Outline each uninfected red blood cell.
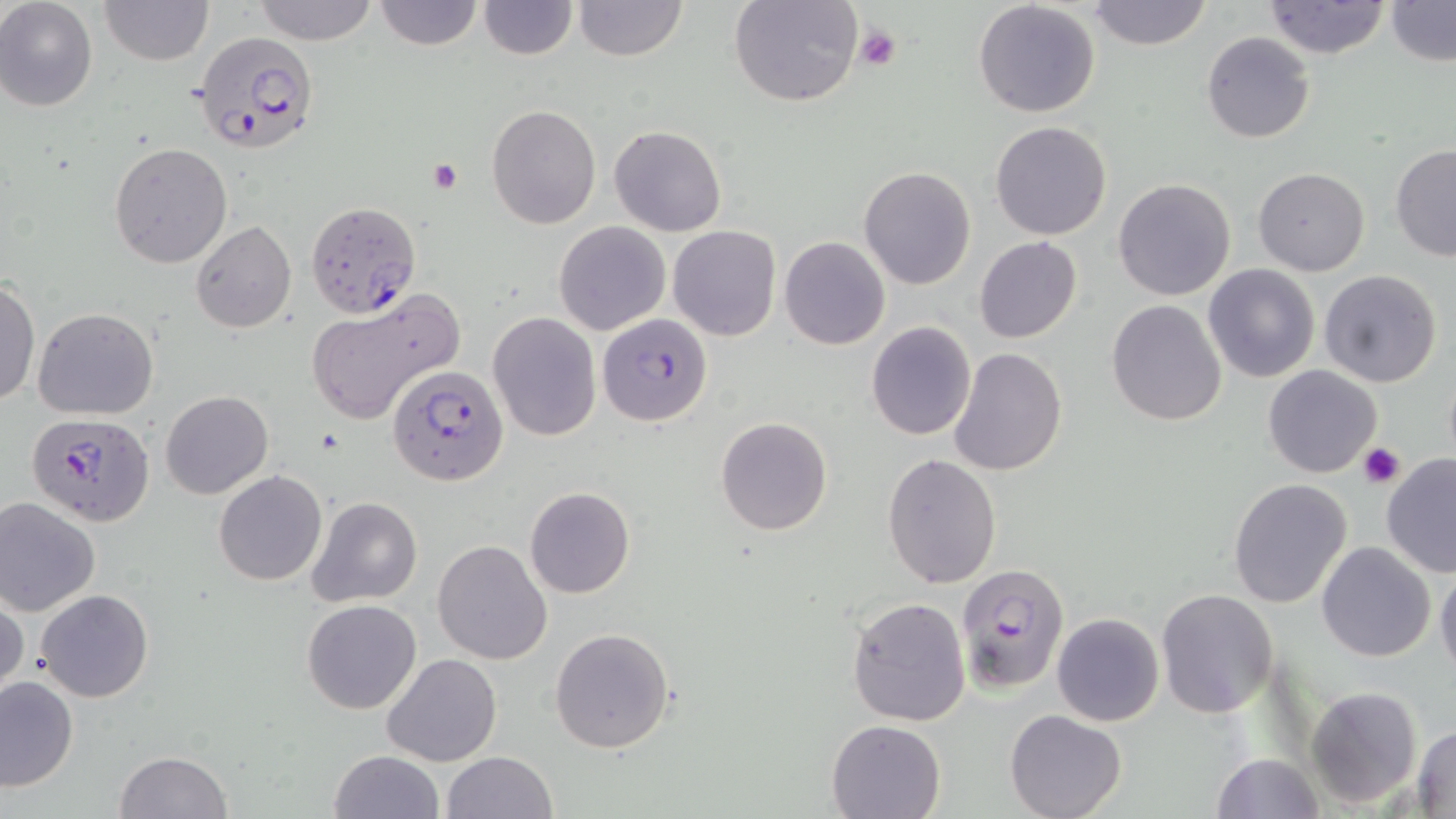
Approximate bounding boxes as (x1, y1, x2, y2) in pixels.
Uninfected red blood cells: (1, 0, 98, 111), (99, 0, 213, 66), (253, 0, 378, 44), (373, 0, 484, 51), (477, 0, 576, 59), (573, 0, 686, 62), (729, 0, 864, 108), (1085, 0, 1213, 50), (1263, 0, 1391, 59), (1384, 0, 1456, 66), (973, 1, 1101, 118), (1201, 31, 1315, 143), (486, 104, 600, 229), (990, 121, 1111, 241), (610, 125, 726, 237), (110, 142, 232, 267), (1391, 145, 1456, 261), (858, 166, 977, 290), (1252, 168, 1369, 276), (1112, 177, 1235, 300), (191, 220, 296, 333), (554, 220, 671, 336), (668, 225, 780, 342), (779, 236, 890, 351), (974, 236, 1083, 343), (1203, 264, 1321, 383), (1318, 270, 1442, 389), (0, 278, 40, 408), (304, 293, 462, 424), (1107, 299, 1227, 426), (32, 307, 159, 421), (486, 311, 600, 441), (866, 321, 976, 440), (950, 348, 1068, 477), (1262, 364, 1382, 479), (161, 390, 272, 498), (715, 417, 832, 535), (881, 453, 1002, 589), (1380, 456, 1456, 579), (213, 470, 326, 586), (1227, 478, 1352, 610), (524, 486, 635, 598), (307, 496, 423, 606), (0, 497, 100, 615), (5, 518, 121, 674), (432, 539, 554, 665), (1316, 541, 1435, 661), (1435, 566, 1456, 682), (35, 588, 153, 702), (1156, 589, 1277, 717), (0, 592, 26, 702), (845, 595, 971, 726), (301, 600, 421, 715), (1051, 612, 1164, 726), (550, 627, 674, 752), (382, 654, 502, 767), (0, 675, 79, 792), (1304, 685, 1421, 808), (1005, 708, 1127, 819), (825, 718, 948, 819), (1412, 726, 1456, 815), (328, 749, 444, 819), (116, 750, 232, 819), (442, 751, 559, 819), (1211, 752, 1323, 819).

slide-level diagnosis = Plasmodium falciparum
magnification = 1000x
modality = light microscopy
Plasmodium falciparum-infected red blood cell locations = approximate bounding boxes as (x1, y1, x2, y2) in pixels: (193, 32, 318, 157), (305, 201, 421, 320), (597, 313, 712, 426), (387, 364, 508, 486), (29, 413, 155, 525), (954, 563, 1071, 693)
field of view = single
stain = May-Grünwald-Giemsa
preparation = thin blood smear
image size = 1456×819 pixels
platelet locations = approximate bounding boxes as (x1, y1, x2, y2) in pixels: (854, 26, 902, 73), (427, 159, 464, 193), (1357, 441, 1405, 489)